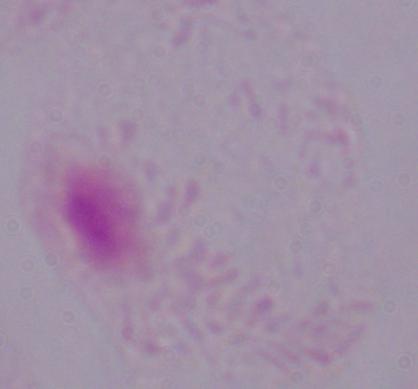

identification: trichomonad
modality: micrograph
magnification: 1000x